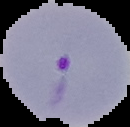

Summary:
  - Image size: 130×127 pixels
  - Result: Plasmodium parasites identified
  - Image type: segmented cell region on a black background
  - Preparation: thin blood film